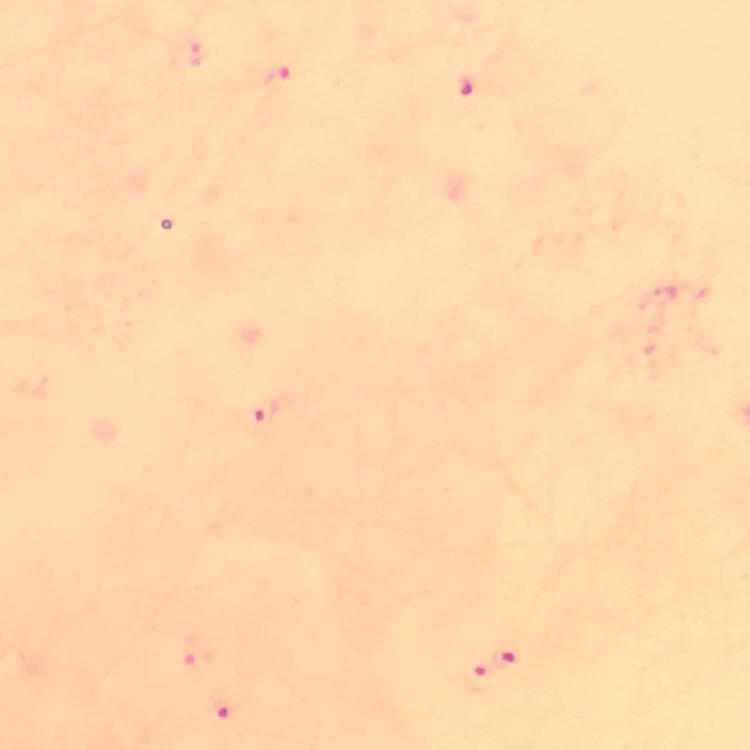

Approximate centers as {x, y} in pixels. Malaria parasite locations: {197, 52}, {278, 78}, {263, 412}, {196, 649}, {507, 658}, {479, 680}, {225, 707}. At 100x magnification. From a malaria diagnostic workup. Thick blood smear. Giemsa-stained preparation. Immersion oil applied. Image is 750×750 pixels. Photographed through the microscope with a smartphone camera. Cropped region of a single field of view.